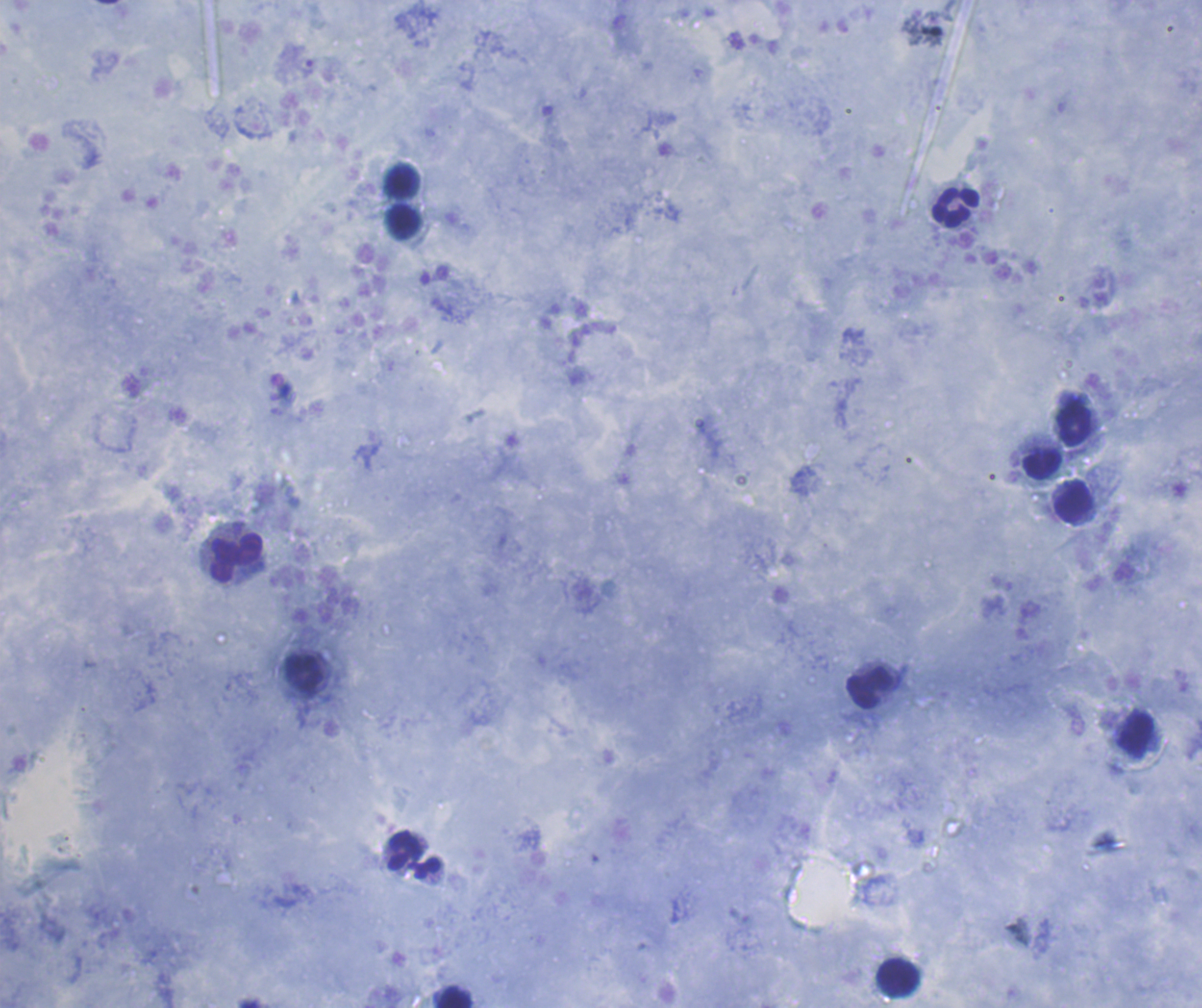

{
  "coloration_quality": "good",
  "context": "previously used in an actual diagnosis",
  "preparation": "thick blood smear",
  "magnification": "100x",
  "result": "no Plasmodium parasites detected",
  "field_of_view": "one from this slide",
  "background_quality": "good",
  "leukocyte_locations": "approximate centers as [x, y] in pixels: [402, 181], [955, 208], [403, 221], [1074, 426], [1042, 464], [1074, 502], [235, 557], [304, 672], [869, 687], [413, 855], [898, 978], [454, 996]",
  "image_size": "1202×1008 pixels",
  "stain": "Romanowsky"
}